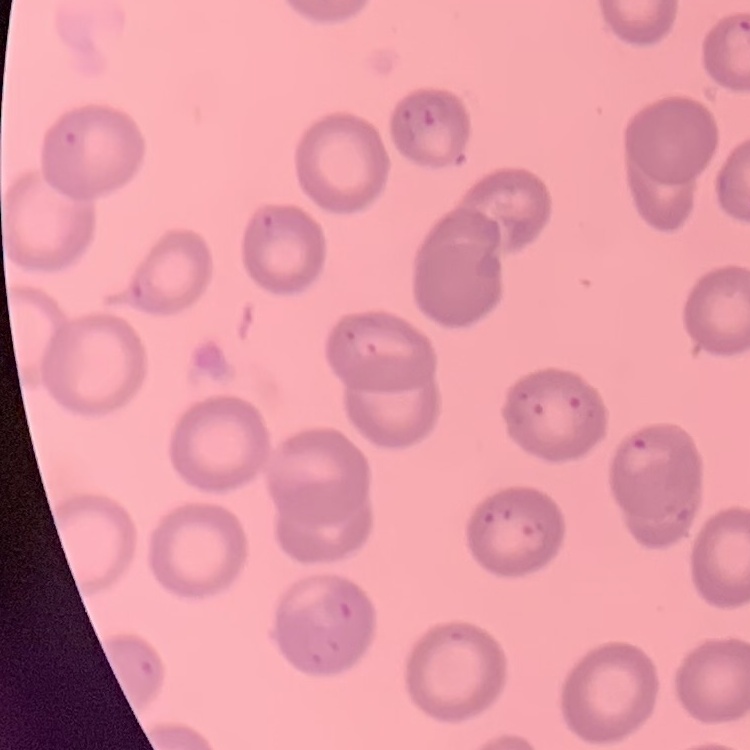

Summary:
  - Red blood cell morphology: no rouleaux formation
  - Stain: Field's or Giemsa
  - Image type: square crop of a larger photomicrograph
  - Preparation: thin blood film